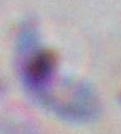 Captured at 1000x magnification. Toxoplasma gondii is seen. Micrograph.